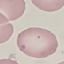
{
  "result": "no malaria parasites seen",
  "capture": "smartphone through the microscope eyepiece",
  "stain": "Giemsa",
  "preparation": "thin blood smear",
  "image_type": "cell patch, automatically extracted from a larger field of view and resized to 64 × 64 pixels"
}